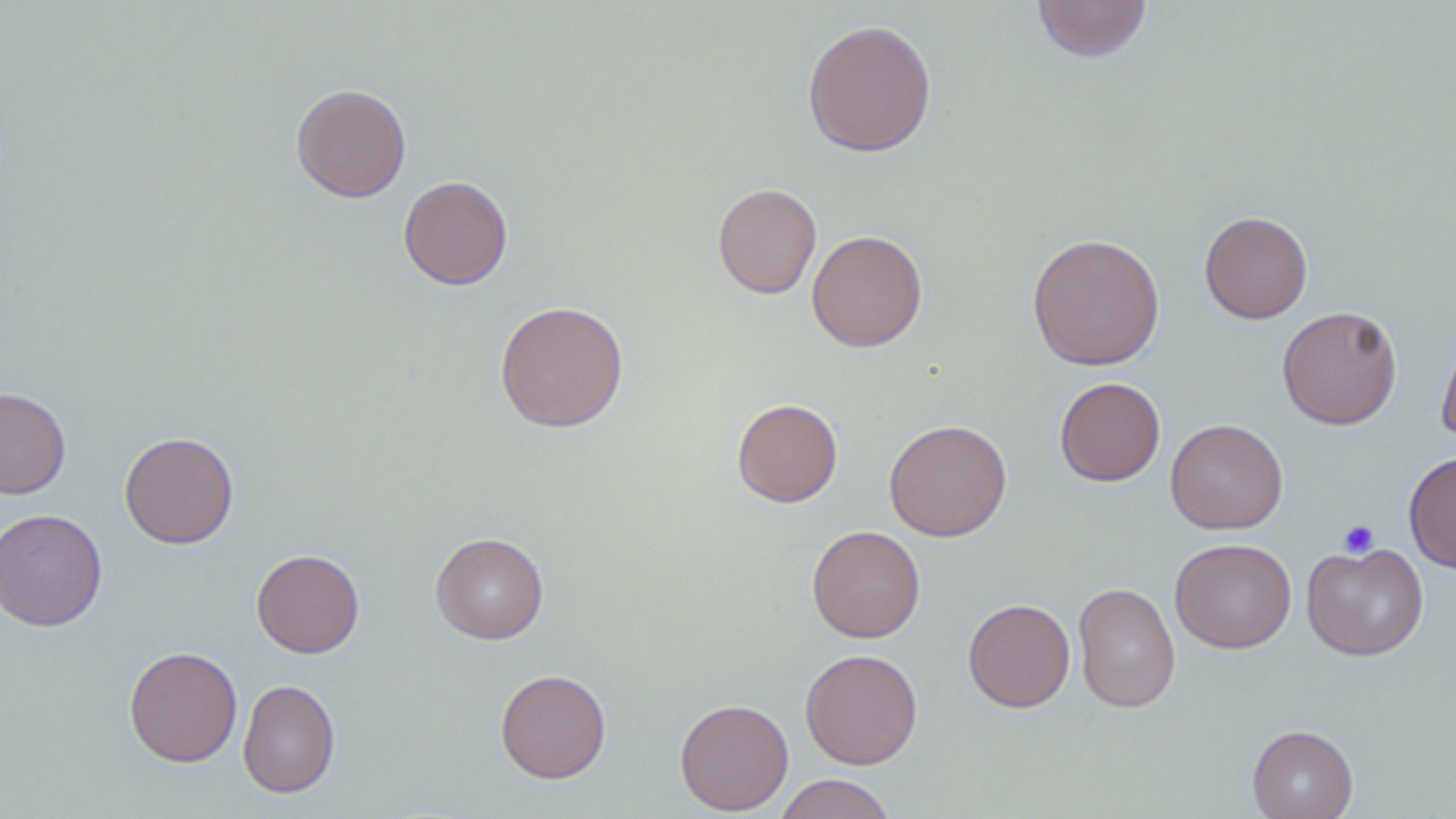
Approximate bounding boxes as (x1,y1)-(x2,y2) corner pairs in pixels. Platelet locations: (1338,519)-(1379,558). Uninfected red blood cell locations: (1031,0)-(1152,62), (801,18)-(937,157), (290,83)-(412,202), (398,175)-(513,290), (712,182)-(822,299), (1199,210)-(1313,323), (806,229)-(928,352), (1026,232)-(1165,371), (494,299)-(629,433), (1277,305)-(1403,430), (1436,324)-(1456,448), (1054,377)-(1165,486), (0,387)-(71,499), (731,398)-(843,507), (1165,418)-(1289,534), (883,419)-(1012,542), (119,431)-(238,549), (1403,450)-(1456,573), (0,508)-(107,632), (806,524)-(925,643), (430,532)-(549,644), (1170,538)-(1297,654), (1301,541)-(1429,661), (251,549)-(364,658), (1072,582)-(1180,713), (962,598)-(1076,712), (123,645)-(242,767), (799,648)-(923,769), (495,668)-(611,784), (238,678)-(340,798), (674,697)-(794,815), (1247,724)-(1358,819), (773,773)-(896,819). Slide-level diagnosis: no evidence of blood parasites. Single field of view. Optical microscopy. May-Grünwald-Giemsa-stained preparation. Thin blood film. Image is 1456×819 pixels. 1000x magnification.